State the blood parasite species.
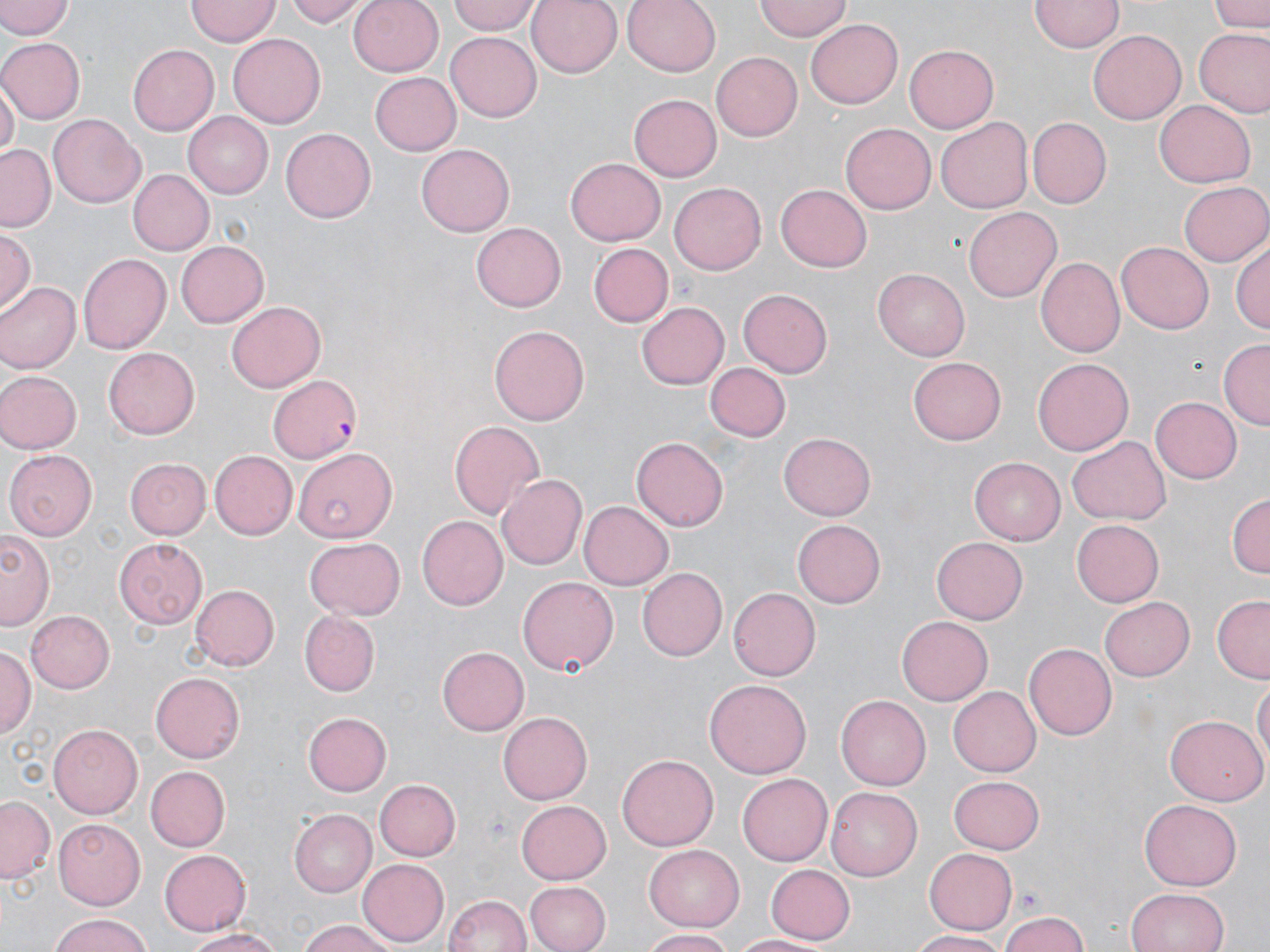

Plasmodium falciparum.

Approximate bounding boxes as named x1/y1/x2/y2 corners in pixels. Plasmodium falciparum-infected red blood cell locations: (x1=268, y1=373, x2=365, y2=463). Uninfected red blood cell locations: (x1=0, y1=0, x2=74, y2=40), (x1=285, y1=0, x2=368, y2=27), (x1=348, y1=0, x2=445, y2=76), (x1=449, y1=0, x2=541, y2=35), (x1=527, y1=0, x2=624, y2=78), (x1=623, y1=0, x2=722, y2=77), (x1=755, y1=0, x2=852, y2=40), (x1=1030, y1=0, x2=1122, y2=53), (x1=1209, y1=0, x2=1267, y2=32), (x1=185, y1=1, x2=280, y2=46), (x1=805, y1=18, x2=903, y2=107), (x1=1195, y1=28, x2=1270, y2=118), (x1=228, y1=31, x2=325, y2=124), (x1=1087, y1=31, x2=1185, y2=124), (x1=445, y1=34, x2=542, y2=120), (x1=0, y1=38, x2=83, y2=123), (x1=903, y1=42, x2=999, y2=134), (x1=128, y1=44, x2=218, y2=136), (x1=710, y1=51, x2=801, y2=139), (x1=372, y1=73, x2=462, y2=156), (x1=1, y1=82, x2=16, y2=163), (x1=628, y1=93, x2=721, y2=182), (x1=1154, y1=101, x2=1254, y2=186), (x1=183, y1=111, x2=273, y2=198), (x1=48, y1=116, x2=147, y2=208), (x1=937, y1=118, x2=1035, y2=212), (x1=1028, y1=118, x2=1112, y2=207), (x1=839, y1=121, x2=935, y2=215), (x1=280, y1=126, x2=374, y2=220), (x1=0, y1=145, x2=55, y2=233), (x1=417, y1=145, x2=516, y2=236), (x1=564, y1=157, x2=665, y2=246), (x1=127, y1=168, x2=213, y2=257), (x1=1180, y1=180, x2=1270, y2=266), (x1=670, y1=183, x2=766, y2=274), (x1=775, y1=183, x2=873, y2=270), (x1=963, y1=205, x2=1061, y2=300), (x1=469, y1=223, x2=565, y2=311), (x1=0, y1=229, x2=37, y2=313), (x1=1232, y1=238, x2=1270, y2=334), (x1=178, y1=241, x2=270, y2=330), (x1=587, y1=242, x2=672, y2=328), (x1=1116, y1=242, x2=1214, y2=334), (x1=77, y1=253, x2=172, y2=355), (x1=1038, y1=256, x2=1127, y2=357), (x1=871, y1=268, x2=970, y2=360), (x1=0, y1=281, x2=78, y2=373), (x1=738, y1=286, x2=832, y2=375), (x1=637, y1=300, x2=730, y2=391), (x1=227, y1=301, x2=327, y2=393), (x1=489, y1=325, x2=589, y2=425), (x1=1220, y1=339, x2=1270, y2=428), (x1=104, y1=345, x2=199, y2=437), (x1=907, y1=358, x2=1006, y2=446), (x1=1033, y1=358, x2=1134, y2=456), (x1=707, y1=362, x2=789, y2=441), (x1=0, y1=369, x2=79, y2=454), (x1=1150, y1=396, x2=1241, y2=484), (x1=448, y1=420, x2=546, y2=520), (x1=777, y1=432, x2=876, y2=521), (x1=632, y1=436, x2=729, y2=530), (x1=1067, y1=436, x2=1171, y2=525), (x1=293, y1=446, x2=397, y2=541), (x1=4, y1=449, x2=99, y2=540), (x1=210, y1=451, x2=297, y2=540), (x1=970, y1=455, x2=1069, y2=545), (x1=126, y1=458, x2=209, y2=539), (x1=498, y1=474, x2=587, y2=569), (x1=1227, y1=492, x2=1269, y2=582), (x1=579, y1=501, x2=674, y2=589), (x1=420, y1=514, x2=509, y2=611), (x1=793, y1=518, x2=887, y2=607), (x1=1072, y1=519, x2=1163, y2=606), (x1=0, y1=529, x2=54, y2=629), (x1=930, y1=536, x2=1028, y2=624), (x1=114, y1=538, x2=209, y2=626), (x1=305, y1=538, x2=404, y2=620), (x1=638, y1=567, x2=728, y2=660), (x1=517, y1=575, x2=618, y2=677), (x1=190, y1=584, x2=277, y2=669), (x1=729, y1=587, x2=821, y2=680), (x1=1099, y1=596, x2=1196, y2=681), (x1=1213, y1=598, x2=1269, y2=681), (x1=26, y1=610, x2=114, y2=693), (x1=298, y1=611, x2=381, y2=696), (x1=897, y1=615, x2=993, y2=705), (x1=0, y1=644, x2=34, y2=740), (x1=1024, y1=644, x2=1116, y2=741), (x1=436, y1=646, x2=528, y2=735), (x1=151, y1=673, x2=245, y2=762), (x1=1253, y1=675, x2=1269, y2=773), (x1=703, y1=679, x2=812, y2=781), (x1=949, y1=686, x2=1041, y2=777), (x1=835, y1=694, x2=930, y2=791), (x1=302, y1=710, x2=391, y2=796), (x1=499, y1=711, x2=591, y2=805), (x1=1166, y1=715, x2=1265, y2=807), (x1=51, y1=723, x2=147, y2=816), (x1=618, y1=753, x2=717, y2=852), (x1=147, y1=766, x2=229, y2=851), (x1=737, y1=773, x2=831, y2=866), (x1=949, y1=774, x2=1044, y2=852), (x1=374, y1=779, x2=460, y2=861), (x1=828, y1=785, x2=926, y2=880), (x1=1, y1=795, x2=54, y2=883), (x1=516, y1=797, x2=612, y2=881), (x1=1139, y1=799, x2=1243, y2=890), (x1=290, y1=809, x2=376, y2=896), (x1=53, y1=818, x2=146, y2=910), (x1=644, y1=843, x2=744, y2=929), (x1=160, y1=847, x2=252, y2=935), (x1=924, y1=849, x2=1017, y2=936), (x1=357, y1=858, x2=448, y2=946), (x1=766, y1=864, x2=857, y2=943), (x1=524, y1=880, x2=609, y2=952), (x1=1125, y1=887, x2=1231, y2=952), (x1=442, y1=893, x2=535, y2=951), (x1=996, y1=910, x2=1091, y2=952), (x1=44, y1=915, x2=159, y2=952), (x1=293, y1=918, x2=401, y2=952), (x1=179, y1=926, x2=289, y2=950), (x1=640, y1=929, x2=740, y2=951), (x1=912, y1=929, x2=1015, y2=951), (x1=731, y1=933, x2=824, y2=952). One field of a larger specimen. Thin blood smear. Image is 1270×952 pixels. Light microscopy. 1000x magnification. May-Grünwald-Giemsa-stained preparation.